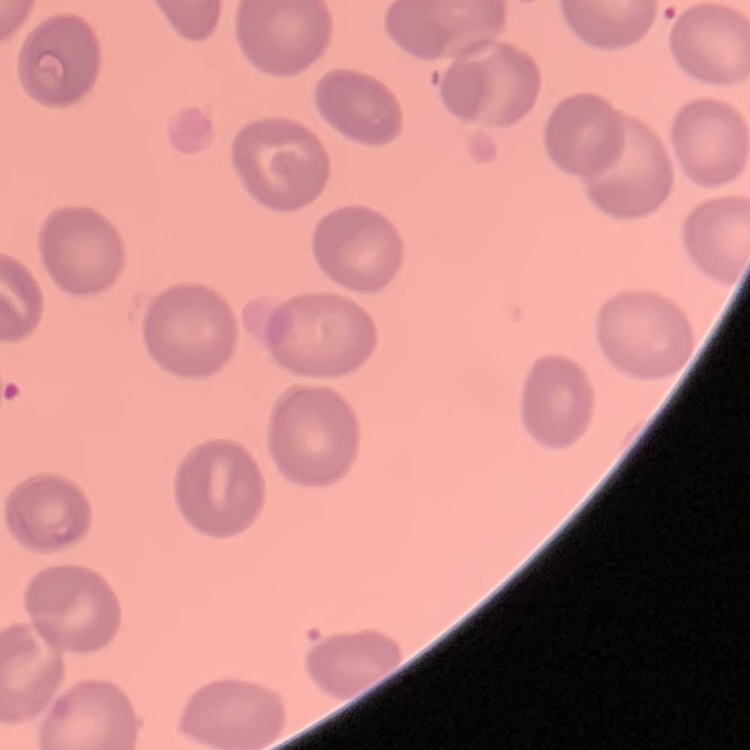
The erythrocytes exhibit no rouleaux formation. Field's or Giemsa stain. Thin peripheral smear. One tile cut from a larger photomicrograph.